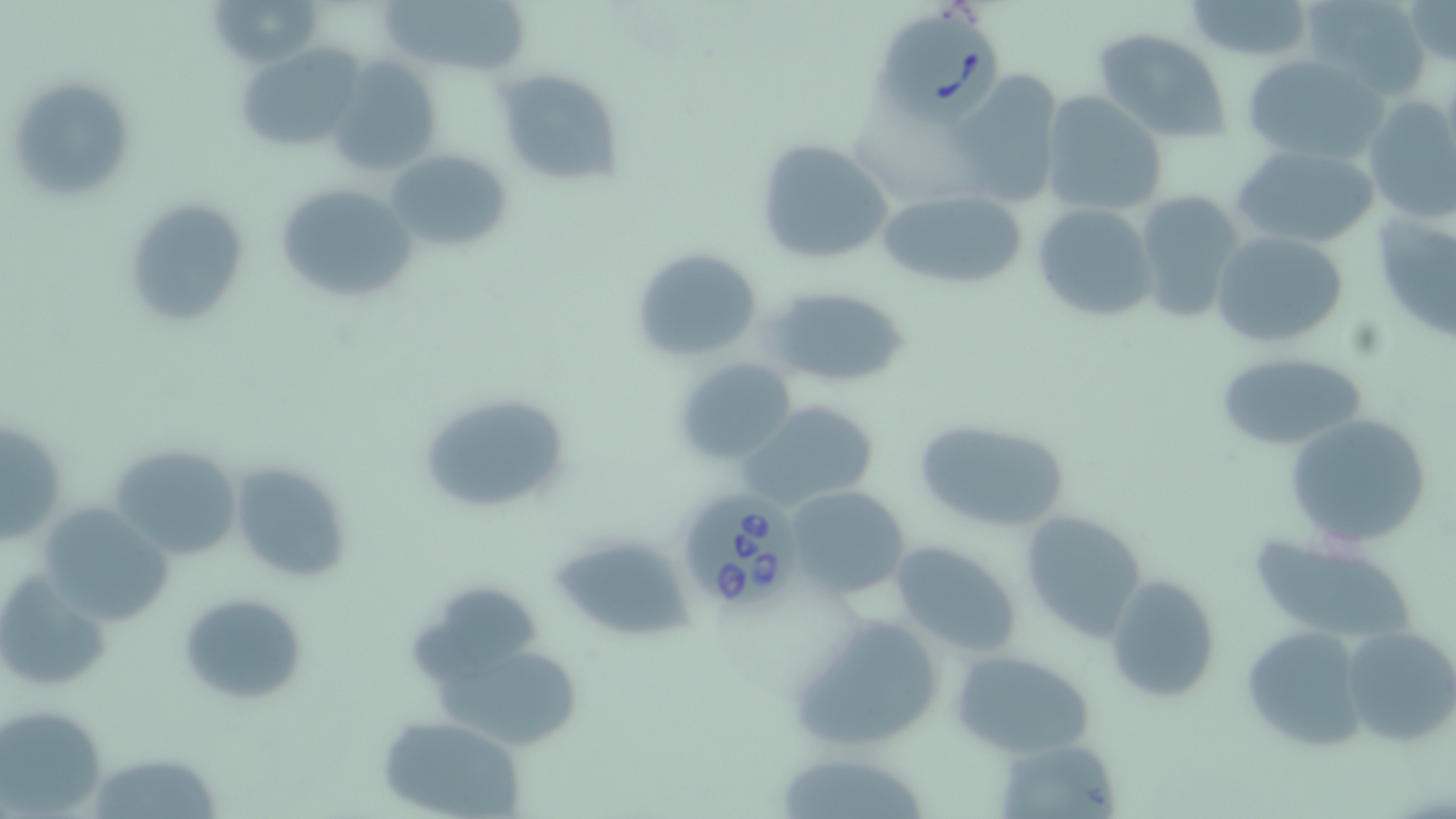
Approximate bounding boxes as named x1/y1/x2/y2 corners in pixels. Uninfected red blood cell locations: (x1=207, y1=0, x2=324, y2=68), (x1=380, y1=0, x2=535, y2=73), (x1=1300, y1=0, x2=1433, y2=97), (x1=1401, y1=0, x2=1455, y2=68), (x1=1182, y1=1, x2=1318, y2=61), (x1=1093, y1=30, x2=1233, y2=143), (x1=236, y1=44, x2=367, y2=149), (x1=1242, y1=53, x2=1389, y2=165), (x1=329, y1=57, x2=444, y2=181), (x1=494, y1=68, x2=625, y2=190), (x1=947, y1=72, x2=1064, y2=207), (x1=4, y1=75, x2=134, y2=203), (x1=1039, y1=91, x2=1169, y2=216), (x1=1361, y1=94, x2=1456, y2=223), (x1=754, y1=136, x2=894, y2=266), (x1=1229, y1=143, x2=1380, y2=250), (x1=386, y1=147, x2=513, y2=256), (x1=273, y1=180, x2=417, y2=304), (x1=875, y1=186, x2=1031, y2=291), (x1=1134, y1=188, x2=1247, y2=322), (x1=1371, y1=195, x2=1456, y2=341), (x1=125, y1=198, x2=250, y2=329), (x1=1031, y1=201, x2=1159, y2=323), (x1=1209, y1=229, x2=1352, y2=349), (x1=629, y1=246, x2=765, y2=362), (x1=762, y1=282, x2=910, y2=391), (x1=1214, y1=351, x2=1369, y2=454), (x1=672, y1=356, x2=798, y2=465), (x1=416, y1=392, x2=574, y2=519), (x1=737, y1=398, x2=881, y2=511), (x1=1283, y1=412, x2=1434, y2=550), (x1=1, y1=416, x2=67, y2=545), (x1=911, y1=417, x2=1072, y2=533), (x1=104, y1=442, x2=242, y2=562), (x1=228, y1=460, x2=355, y2=586), (x1=784, y1=485, x2=910, y2=599), (x1=37, y1=503, x2=173, y2=626), (x1=1018, y1=510, x2=1147, y2=642), (x1=552, y1=532, x2=692, y2=642), (x1=1246, y1=533, x2=1419, y2=648), (x1=890, y1=541, x2=1023, y2=658), (x1=1103, y1=575, x2=1221, y2=702), (x1=178, y1=592, x2=306, y2=707), (x1=786, y1=612, x2=946, y2=756), (x1=1240, y1=624, x2=1369, y2=754), (x1=1341, y1=626, x2=1456, y2=748), (x1=952, y1=650, x2=1098, y2=758), (x1=436, y1=655, x2=583, y2=745), (x1=2, y1=702, x2=110, y2=816), (x1=378, y1=714, x2=529, y2=818), (x1=996, y1=741, x2=1123, y2=819), (x1=98, y1=753, x2=221, y2=819), (x1=782, y1=758, x2=927, y2=817). Babesia divergens-infected red blood cell locations: (x1=873, y1=5, x2=1008, y2=121), (x1=678, y1=491, x2=802, y2=612). Slide-level diagnosis: Babesia divergens. Single field of view. Image is 1456×819 pixels. May-Grünwald-Giemsa stain. 1000x magnification. Thin blood film. Optical microscopy.